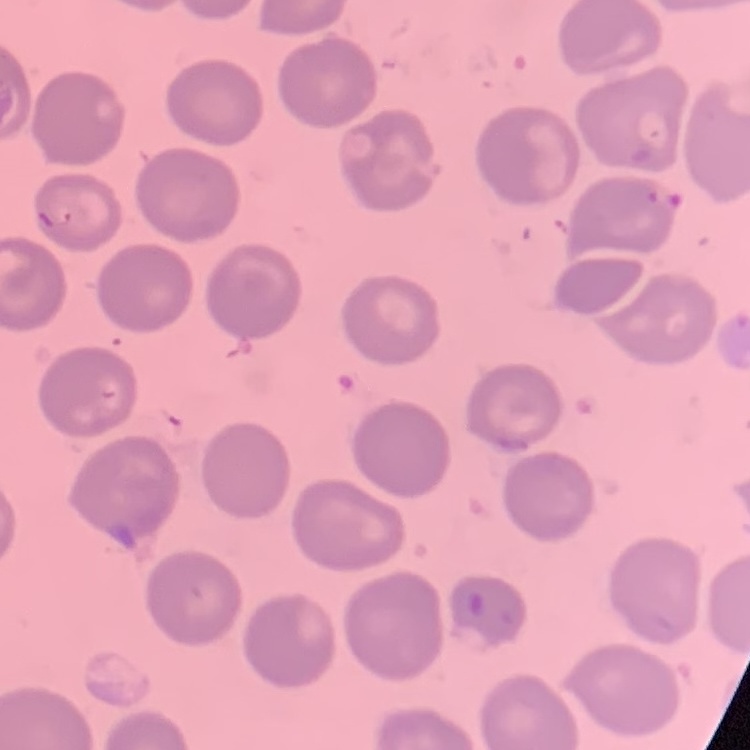
{
  "erythrocyte_morphology": "no rouleaux formation",
  "stain": "Field's or Giemsa",
  "preparation": "thin blood smear",
  "image_type": "one tile cut from a larger photomicrograph"
}